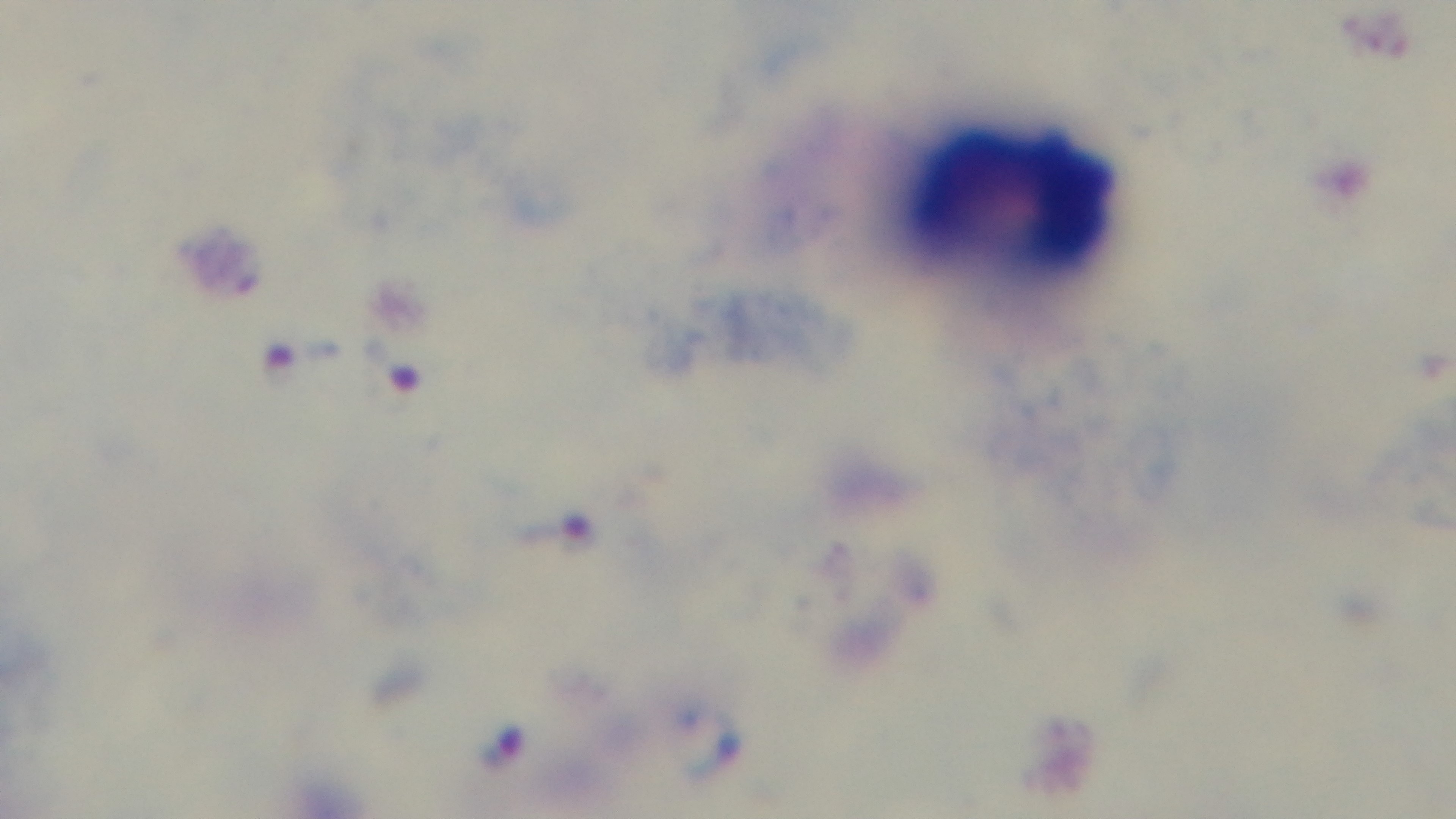

capture = mounted 4K digital camera
malaria status = infected
preparation = thick blood film
stain = Giemsa
objective = 100x oil immersion
modality = light microscopy
field of view = single